Classify this cell by malaria status.
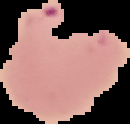

Parasitized.

Summary:
  - Image type: cell region segmented out of the field of view; surrounding area masked to black
  - Preparation: thin blood smear
  - Image size: 130×124 pixels